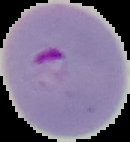
Image is 130×142 pixels. The area outside the segmented cell region is set to black. From a thin blood smear. Malaria status: parasitized.